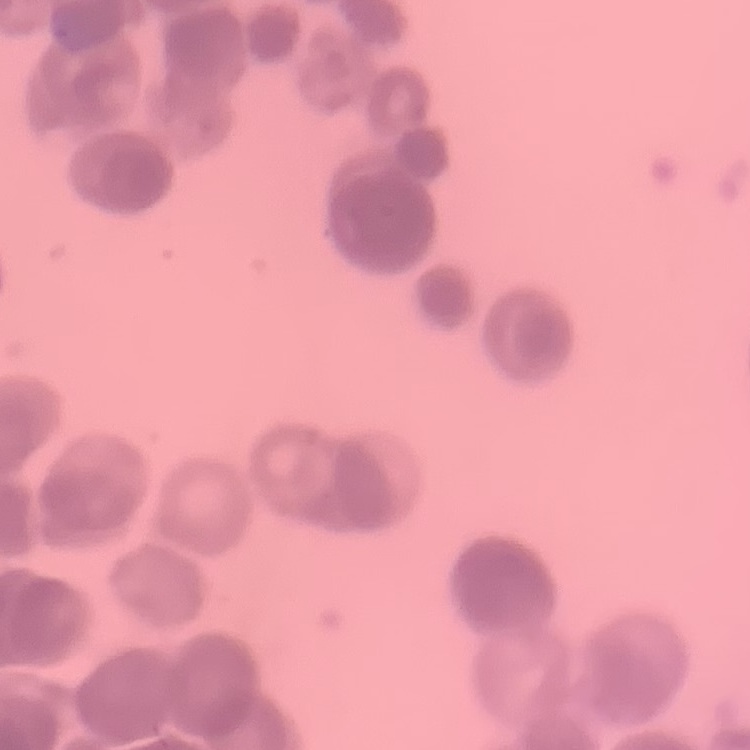
{
  "erythrocyte_morphology": "rouleaux formation",
  "stain": "Field's or Giemsa",
  "image_type": "square crop of a larger photomicrograph",
  "preparation": "thin peripheral smear"
}